Give the extent of the malaria parasites you find, grouped by life-cycle stage — ring form, trophozoite, schizont, or gametocyte.
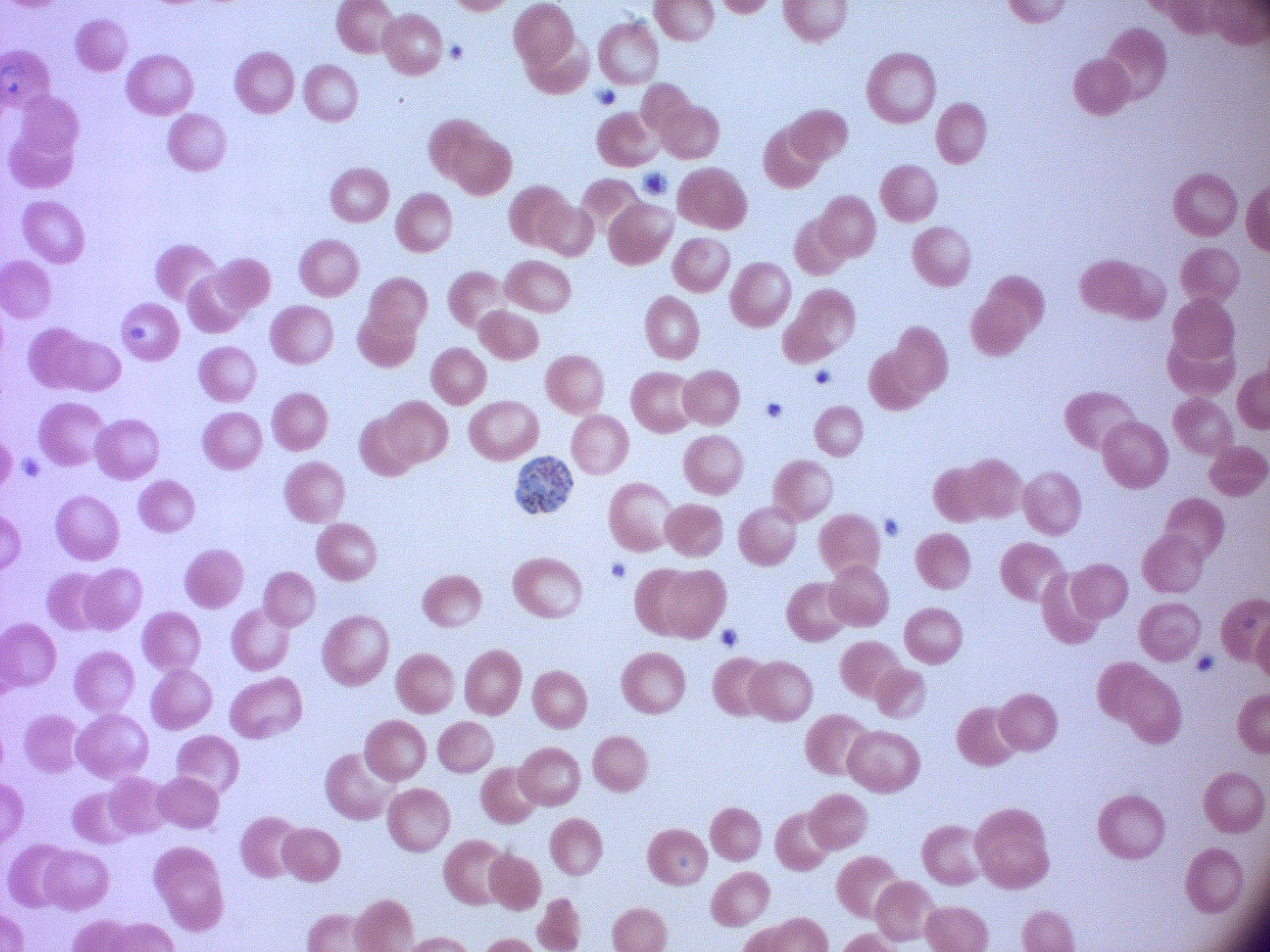

Approximate bounding boxes as (x1,y1)-(x2,y2) corner pairs in pixels, from the source annotation, which is not necessarily exhaustive.
Schizonts: (515,456)-(574,514).

Summary:
  - Image size: 1270×952 pixels
  - Preparation: thin blood smear
  - Microscope: Leica DM2000 with built-in camera
  - Stain: Giemsa
  - Magnification: 100x
  - Field of view: single
  - Species: Plasmodium falciparum